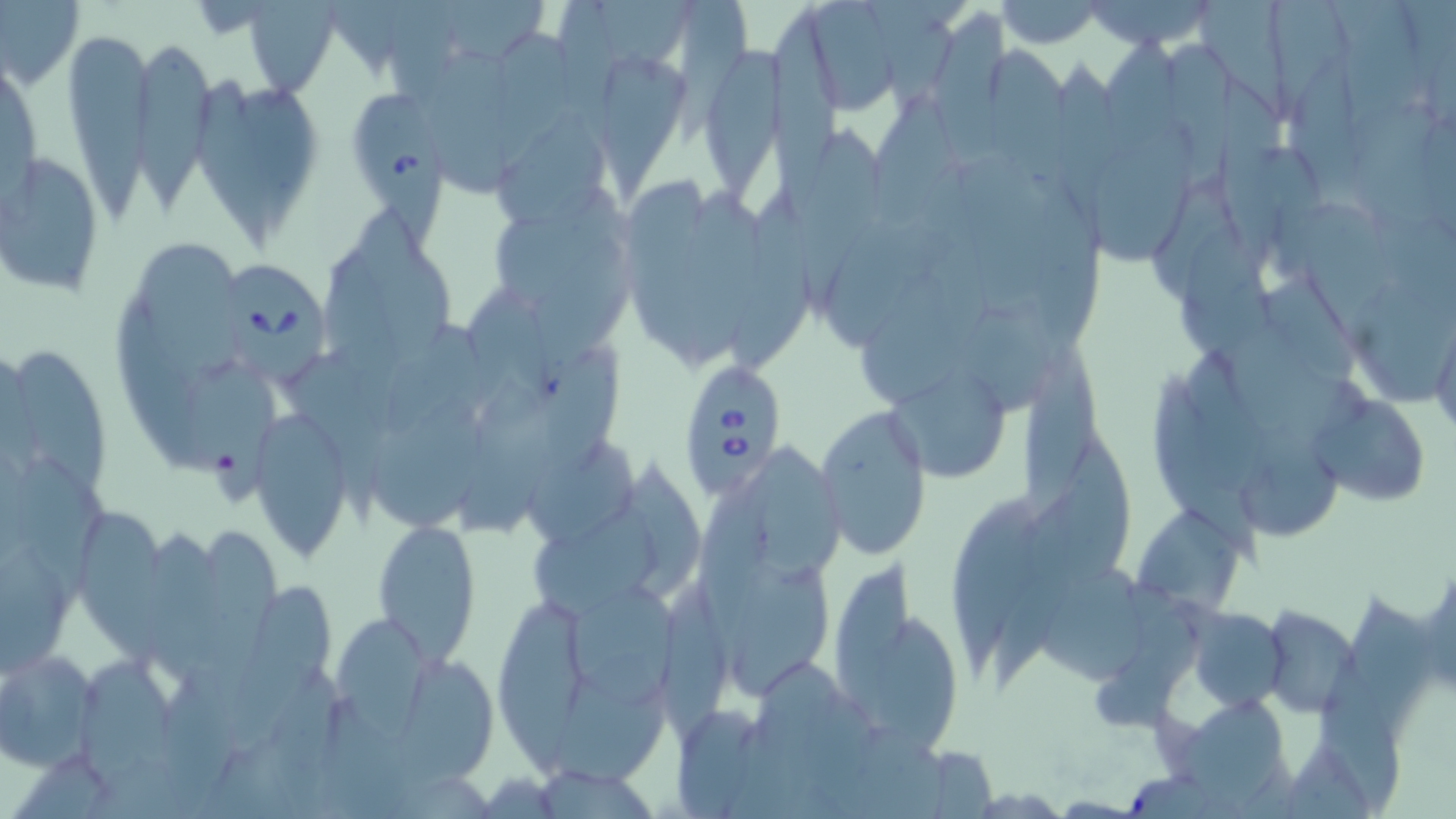 Approximate bounding boxes as (x1,y1)-(x2,y2) corner pairs in pixels. Babesia divergens-infected red blood cell locations: (231,256)-(326,390), (678,362)-(789,498). Uninfected red blood cell locations: (0,0)-(84,88), (244,0)-(340,97), (432,0)-(552,69), (595,0)-(697,79), (808,0)-(898,120), (872,0)-(961,100), (995,0)-(1106,49), (1082,0)-(1222,50), (1202,0)-(1296,124), (1273,0)-(1350,102), (681,1)-(751,133), (769,4)-(845,213), (933,9)-(1013,169), (63,22)-(154,226), (498,29)-(575,181), (136,34)-(217,210), (989,42)-(1072,195), (706,47)-(784,208), (426,53)-(515,193), (606,58)-(693,202), (197,72)-(279,245), (1217,84)-(1287,270), (355,89)-(446,252), (497,116)-(607,232), (1090,121)-(1200,266), (797,129)-(883,310), (2,149)-(107,297), (628,178)-(711,358), (736,185)-(816,369), (1036,187)-(1103,359), (687,189)-(759,360), (502,191)-(627,304), (1301,200)-(1392,354), (356,205)-(456,366), (828,217)-(935,351), (1181,222)-(1266,365), (138,244)-(247,377), (864,268)-(965,405), (1267,273)-(1363,388), (1360,276)-(1451,406), (469,289)-(555,423), (119,297)-(216,475), (970,311)-(1056,409), (384,322)-(484,436), (290,342)-(393,519), (538,342)-(623,483), (13,343)-(113,497), (1015,350)-(1105,526), (204,366)-(286,505), (877,366)-(1011,480), (1151,369)-(1262,566), (369,390)-(492,534), (1316,390)-(1433,509), (815,404)-(930,557), (251,406)-(356,558), (1248,426)-(1336,541), (1054,436)-(1133,587), (527,437)-(641,542), (747,448)-(846,575), (17,457)-(113,599), (703,472)-(776,659), (951,493)-(1043,677), (535,502)-(661,616), (1136,505)-(1247,617), (81,513)-(165,676), (206,521)-(283,698), (373,521)-(480,666), (147,527)-(236,696), (836,557)-(915,728), (728,560)-(832,697), (1056,570)-(1150,682), (660,576)-(722,757), (229,583)-(336,748), (564,583)-(680,710), (496,592)-(590,769), (1262,604)-(1361,717), (1189,607)-(1286,710), (336,612)-(433,742), (881,613)-(961,760), (0,648)-(101,770), (563,650)-(671,787), (760,652)-(852,775), (83,653)-(183,792), (403,655)-(499,792), (1185,692)-(1293,812). Slide-level diagnosis: Babesia divergens. Single field of view. May-Grünwald-Giemsa-stained preparation. Captured at 1000x magnification. Image is 1456×819 pixels. Thin blood smear. Optical microscopy.